Give the position of every leukocyte visible.
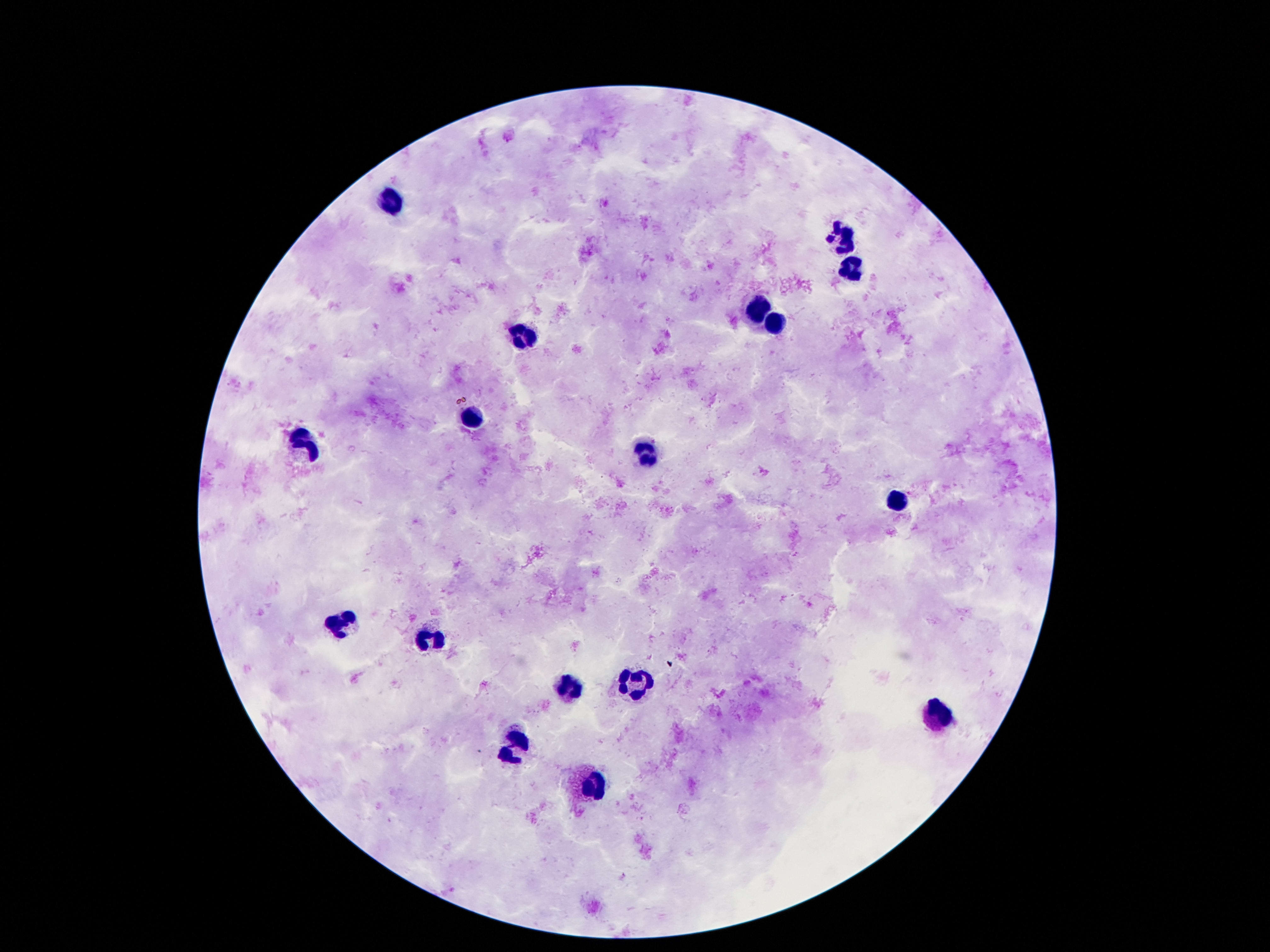

Approximate object centers, in pixels from the top-left corner.
Leukocytes: (x=391, y=202), (x=844, y=235), (x=851, y=265), (x=758, y=309), (x=773, y=320), (x=523, y=336), (x=470, y=422), (x=298, y=443), (x=645, y=450), (x=895, y=504), (x=344, y=622), (x=429, y=642), (x=634, y=684), (x=567, y=687), (x=937, y=716), (x=515, y=748), (x=590, y=784).

preparation: thick blood film
stain: Giemsa
magnification: 100x
capture: smartphone camera through the microscope eyepiece
image_size: 1270×952 pixels
patient_malaria_status: not infected
field_of_view: single